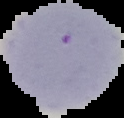 Image is 124×118 pixels. Cell region segmented out of the field of view; the surrounding area is masked to black. Result: negative for malaria parasites. From a thin blood film.